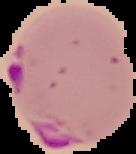
image size = 136×154 pixels
preparation = thin blood film
result = Plasmodium parasites detected
image type = segmented cell region with the area outside set to black